Describe the morphology of the erythrocytes.
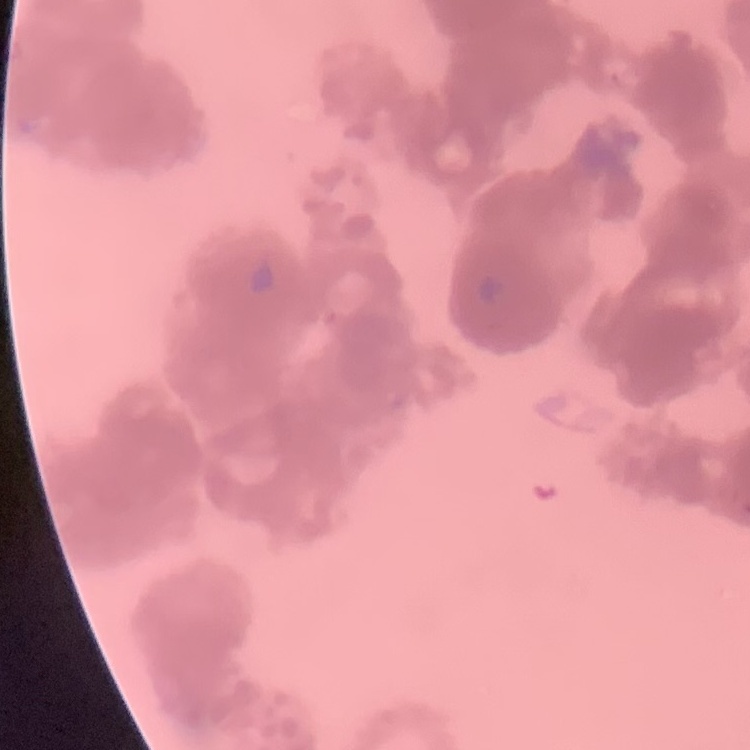
Rouleaux formation.

Square crop of a larger photomicrograph. Thin blood smear. Stained with either Field's or Giemsa.